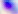
Summary:
  - Magnification: 400x
  - Modality: photomicrograph
  - Identification: Toxoplasma gondii